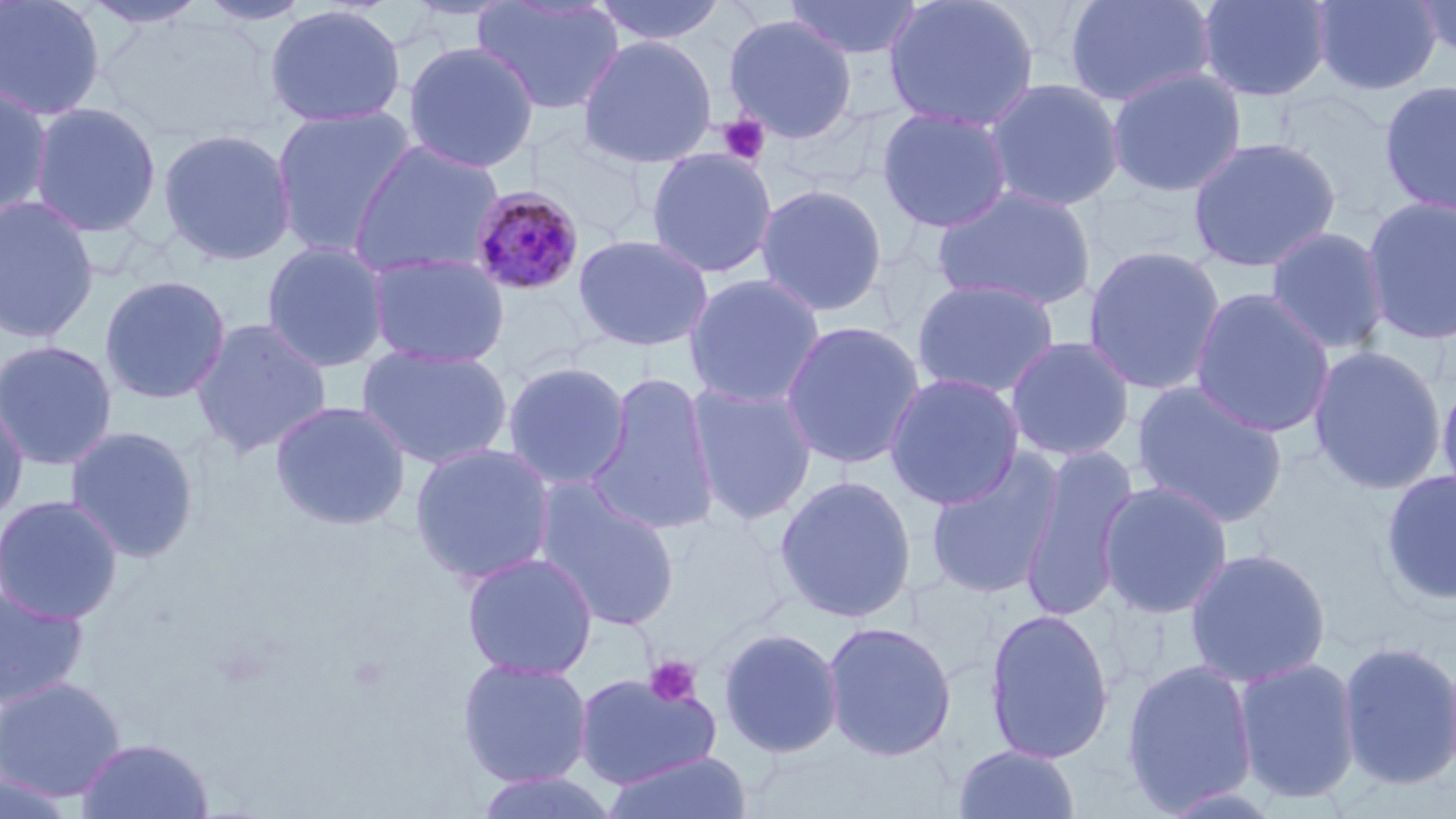
Approximate bounding boxes as (x1,y1)-(x2,y2) corner pairs in pixels. Platelet locations: (717,113)-(771,167), (643,655)-(702,708). Plasmodium malariae-infected red blood cell locations: (468,184)-(586,297). Uninfected red blood cell locations: (0,0)-(107,120), (79,0)-(211,29), (196,0)-(314,27), (473,0)-(626,117), (589,0)-(730,48), (785,0)-(925,61), (882,0)-(1041,133), (1063,0)-(1217,109), (1195,0)-(1333,103), (1310,0)-(1443,96), (1413,0)-(1456,65), (264,3)-(406,129), (723,13)-(859,144), (578,34)-(718,168), (402,41)-(541,173), (1105,67)-(1248,198), (982,77)-(1126,213), (1378,79)-(1456,216), (0,81)-(54,218), (28,101)-(163,238), (270,105)-(417,258), (875,105)-(1013,234), (526,126)-(654,242), (157,127)-(298,267), (1187,135)-(1342,273), (348,140)-(506,280), (644,148)-(778,279), (754,183)-(889,317), (931,185)-(1097,312), (1361,194)-(1456,345), (0,195)-(100,343), (1264,226)-(1391,355), (573,233)-(714,352), (260,240)-(392,373), (1082,245)-(1228,396), (366,251)-(511,369), (684,273)-(826,409), (98,274)-(232,405), (911,277)-(1061,400), (1189,288)-(1335,438), (191,318)-(333,458), (780,320)-(926,471), (1004,335)-(1136,462), (0,339)-(119,471), (356,344)-(513,470), (1308,345)-(1446,495), (501,360)-(632,490), (586,370)-(722,536), (884,372)-(1026,510), (1436,372)-(1456,511), (1130,380)-(1289,529), (686,381)-(818,525), (0,395)-(29,527), (270,399)-(412,530), (63,425)-(200,564), (409,442)-(557,586), (1018,442)-(1140,622), (924,448)-(1065,602), (1380,469)-(1456,606), (774,474)-(918,623), (533,480)-(681,631), (1097,480)-(1234,620), (0,493)-(124,624), (1183,546)-(1332,688), (461,551)-(599,680), (0,585)-(90,708), (983,606)-(1115,765), (822,620)-(958,762), (717,626)-(844,759), (1337,640)-(1456,790), (1232,656)-(1362,804), (456,657)-(594,788), (1121,659)-(1258,815), (573,671)-(722,791), (0,676)-(125,801), (75,736)-(215,819), (952,744)-(1082,819), (600,750)-(752,819), (470,771)-(620,819), (0,772)-(79,818). Slide-level diagnosis: Plasmodium malariae. 1000x magnification. May-Grünwald-Giemsa stain. Image is 1456×819 pixels. Thin blood smear. Light microscopy. Single field of view.